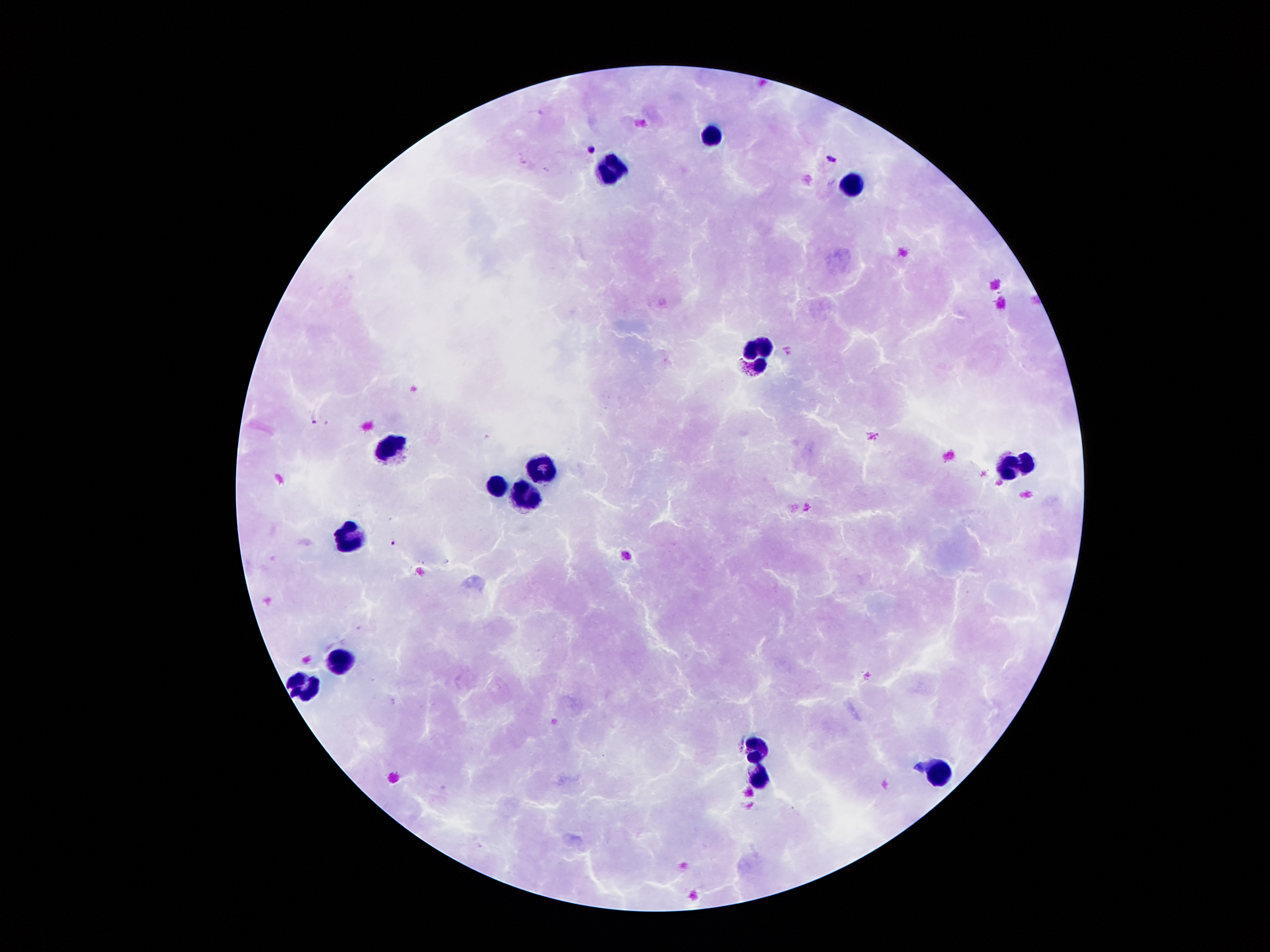

Approximate centers as (x, y) in pixels.
Summary:
  - Plasmodium parasite locations: (541, 112), (591, 148), (521, 160), (831, 160), (830, 181), (314, 421), (393, 543)
  - Leukocyte locations: (709, 135), (610, 169), (854, 189), (756, 354), (390, 448), (1016, 467), (541, 469), (498, 487), (526, 495), (345, 539), (343, 662), (304, 691), (756, 750), (937, 777), (760, 781)
  - Patient malaria status: positive for Plasmodium falciparum
  - Capture: smartphone through the microscope eyepiece
  - Stain: Giemsa
  - Preparation: thick blood smear
  - Image size: 1270×952 pixels
  - Magnification: 100x
  - Field of view: one from this slide